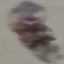

Summary:
  - Result: malaria parasites identified
  - Image type: automatically extracted cell patch, resized to 64 × 64 pixels
  - Preparation: thin blood smear
  - Capture: smartphone camera at the microscope eyepiece
  - Stain: Giemsa